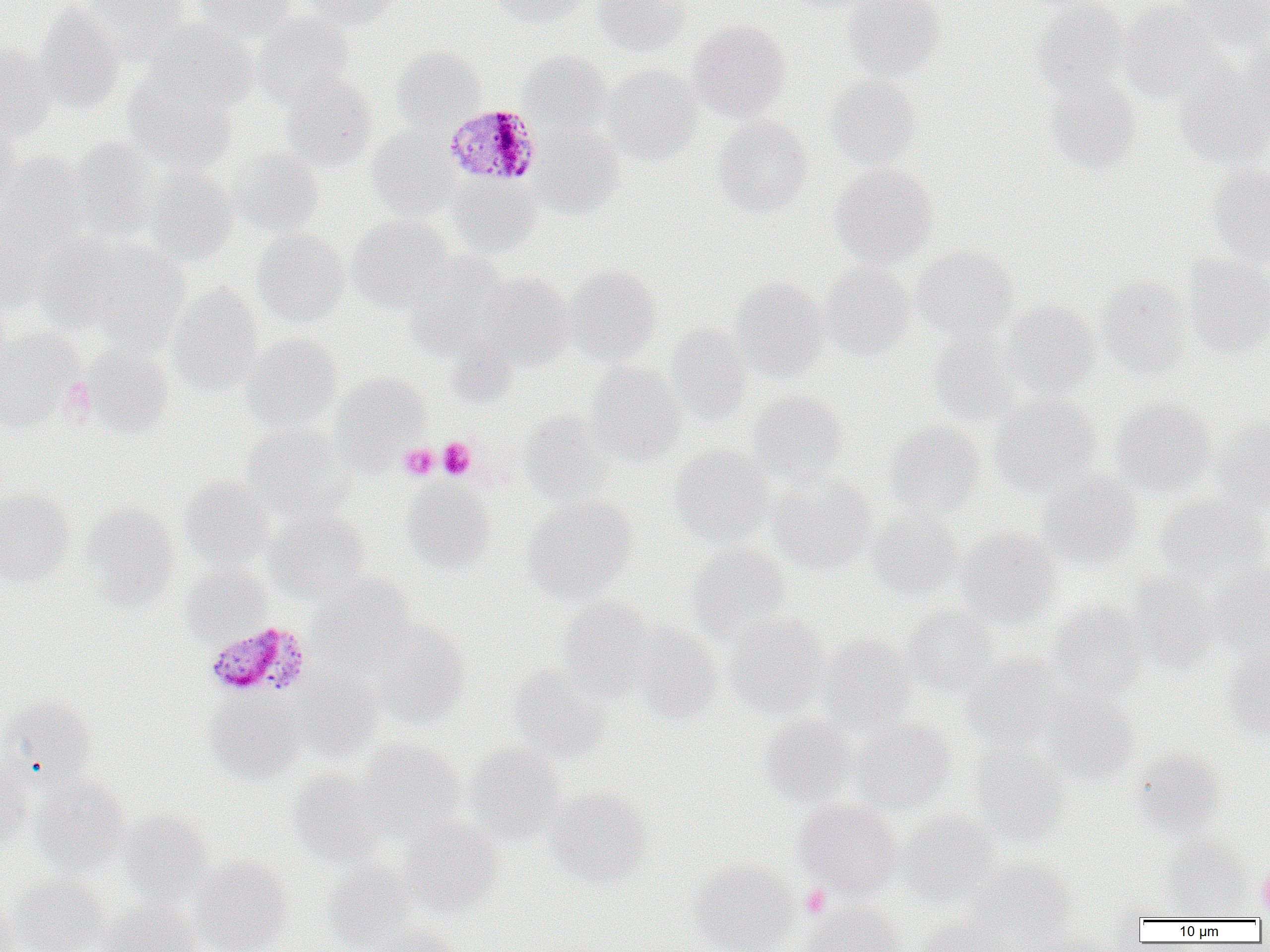

{
  "slide_level_diagnosis": "Plasmodium malariae",
  "field_of_view": "one of a larger specimen",
  "uninfected_red_blood_cell_locations": "approximate bounding boxes as (x1, y1, x2, y2) in pixels: (83, 0, 191, 60), (193, 0, 295, 41), (302, 0, 399, 28), (493, 0, 588, 29), (591, 0, 692, 56), (782, 0, 881, 14), (842, 0, 946, 81), (1183, 0, 1270, 47), (1032, 1, 1130, 99), (35, 3, 124, 114), (1118, 3, 1223, 103), (252, 14, 355, 108), (688, 19, 790, 120), (143, 22, 257, 113), (1241, 27, 1269, 129), (0, 43, 56, 140), (392, 46, 485, 130), (518, 52, 612, 135), (1176, 64, 1270, 168), (604, 65, 700, 163), (281, 71, 378, 169), (124, 75, 238, 175), (826, 75, 921, 169), (1041, 77, 1143, 172), (0, 113, 22, 210), (714, 117, 812, 216), (531, 126, 624, 217), (368, 127, 460, 218), (68, 137, 160, 240), (227, 148, 324, 237), (1, 154, 89, 254), (830, 164, 938, 266), (1206, 165, 1270, 266), (145, 167, 238, 265), (448, 175, 542, 257), (347, 215, 454, 312), (0, 228, 45, 317), (252, 229, 349, 326), (37, 235, 142, 332), (83, 242, 189, 351), (912, 247, 1020, 341), (404, 254, 508, 358), (1183, 255, 1270, 356), (820, 263, 915, 360), (564, 267, 662, 364), (478, 273, 573, 368), (1097, 277, 1191, 377), (730, 278, 831, 381), (168, 284, 263, 394), (1000, 301, 1099, 395), (666, 323, 752, 427), (0, 329, 80, 432), (930, 330, 1021, 426), (242, 334, 342, 431), (82, 344, 174, 437), (587, 362, 687, 464), (332, 373, 430, 463), (748, 391, 848, 483), (990, 395, 1101, 496), (1111, 398, 1216, 495), (520, 412, 615, 503), (1212, 415, 1270, 514), (885, 423, 986, 520), (240, 424, 352, 518), (670, 447, 773, 546), (769, 475, 877, 572), (1037, 475, 1144, 568), (181, 478, 275, 567), (402, 482, 497, 572), (0, 487, 74, 587), (1153, 494, 1269, 587), (523, 497, 636, 603), (81, 503, 180, 607), (867, 509, 961, 600), (265, 510, 368, 602), (953, 527, 1061, 628), (686, 544, 793, 643), (1209, 560, 1270, 659), (181, 565, 271, 643), (1126, 574, 1219, 672), (312, 577, 418, 670), (557, 598, 655, 698), (1048, 601, 1148, 700), (902, 605, 998, 697), (724, 614, 830, 718), (373, 621, 472, 728), (631, 625, 724, 722), (818, 635, 919, 732), (1224, 647, 1270, 740), (961, 653, 1064, 749), (508, 664, 610, 761), (291, 670, 384, 760), (1039, 689, 1140, 785), (1, 695, 98, 784), (206, 696, 305, 784), (760, 715, 858, 803), (852, 719, 955, 813), (359, 740, 465, 837), (970, 742, 1069, 843), (465, 744, 566, 844), (1132, 749, 1225, 838), (0, 756, 33, 849), (287, 770, 386, 867), (32, 775, 130, 875), (545, 788, 651, 887), (795, 797, 901, 896), (897, 811, 999, 906), (120, 812, 214, 905), (399, 819, 502, 916), (1162, 837, 1252, 918), (192, 857, 294, 952), (968, 859, 1078, 947), (689, 861, 799, 952), (322, 862, 419, 950), (7, 874, 108, 952), (0, 898, 27, 952), (96, 901, 200, 952), (800, 904, 908, 952), (915, 918, 1011, 952), (377, 925, 464, 952)",
  "image_size": "1270×952 pixels",
  "modality": "optical microscopy",
  "preparation": "thin blood smear",
  "plasmodium_malariae_infected_red_blood_cell_locations": "approximate bounding boxes as (x1, y1, x2, y2) in pixels: (444, 103, 541, 185), (203, 621, 313, 700)",
  "magnification": "1000x",
  "platelet_locations": "approximate bounding boxes as (x1, y1, x2, y2) in pixels: (59, 376, 96, 424), (438, 438, 475, 479), (398, 443, 438, 480), (1257, 862, 1270, 915), (800, 884, 831, 918)"
}